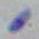
1000x magnification. Photomicrograph. Toxoplasma gondii is seen.